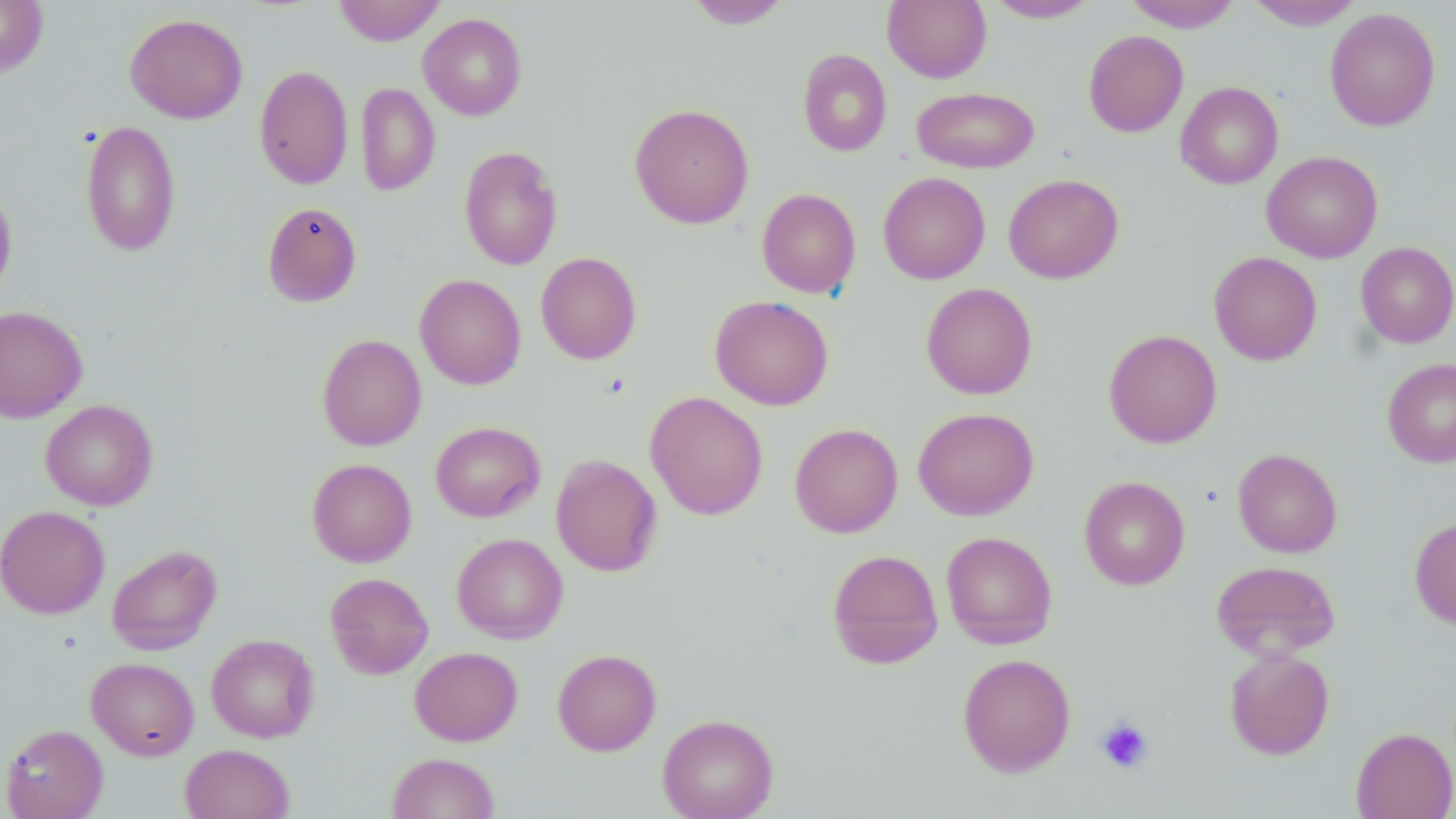

Approximate bounding boxes as named x1/y1/x2/y2 corners in pixels. Platelet locations: (x1=1096, y1=716, x2=1154, y2=774). Uninfected red blood cell locations: (x1=0, y1=0, x2=48, y2=76), (x1=333, y1=0, x2=445, y2=46), (x1=684, y1=0, x2=793, y2=29), (x1=882, y1=0, x2=991, y2=83), (x1=986, y1=0, x2=1100, y2=23), (x1=1124, y1=0, x2=1241, y2=32), (x1=1246, y1=0, x2=1364, y2=30), (x1=1324, y1=7, x2=1440, y2=132), (x1=125, y1=13, x2=248, y2=124), (x1=418, y1=13, x2=527, y2=121), (x1=1083, y1=30, x2=1188, y2=137), (x1=797, y1=49, x2=892, y2=157), (x1=254, y1=64, x2=353, y2=190), (x1=1175, y1=81, x2=1284, y2=189), (x1=356, y1=82, x2=440, y2=196), (x1=911, y1=86, x2=1039, y2=173), (x1=629, y1=102, x2=754, y2=230), (x1=80, y1=119, x2=182, y2=257), (x1=459, y1=146, x2=562, y2=270), (x1=1261, y1=151, x2=1383, y2=263), (x1=878, y1=171, x2=991, y2=284), (x1=1003, y1=173, x2=1124, y2=284), (x1=0, y1=183, x2=18, y2=299), (x1=757, y1=188, x2=861, y2=298), (x1=262, y1=201, x2=362, y2=307), (x1=1355, y1=242, x2=1456, y2=348), (x1=536, y1=251, x2=641, y2=364), (x1=1208, y1=251, x2=1322, y2=366), (x1=414, y1=273, x2=526, y2=390), (x1=921, y1=283, x2=1037, y2=399), (x1=710, y1=295, x2=833, y2=410), (x1=0, y1=305, x2=88, y2=422), (x1=1103, y1=329, x2=1222, y2=449), (x1=317, y1=334, x2=426, y2=451), (x1=1382, y1=359, x2=1456, y2=467), (x1=645, y1=391, x2=768, y2=520), (x1=40, y1=399, x2=158, y2=511), (x1=913, y1=407, x2=1039, y2=520), (x1=430, y1=421, x2=544, y2=522), (x1=789, y1=422, x2=903, y2=537), (x1=1232, y1=448, x2=1342, y2=558), (x1=551, y1=453, x2=662, y2=577), (x1=307, y1=458, x2=417, y2=567), (x1=1079, y1=476, x2=1190, y2=590), (x1=0, y1=505, x2=110, y2=618), (x1=1410, y1=517, x2=1456, y2=630), (x1=941, y1=531, x2=1058, y2=649), (x1=452, y1=532, x2=568, y2=643), (x1=106, y1=544, x2=222, y2=655), (x1=826, y1=549, x2=944, y2=669), (x1=1211, y1=560, x2=1340, y2=661), (x1=325, y1=572, x2=434, y2=679), (x1=206, y1=633, x2=319, y2=742), (x1=410, y1=646, x2=523, y2=746), (x1=552, y1=648, x2=661, y2=756), (x1=1224, y1=648, x2=1335, y2=760), (x1=957, y1=653, x2=1076, y2=776), (x1=86, y1=657, x2=199, y2=759), (x1=657, y1=713, x2=779, y2=819), (x1=0, y1=724, x2=108, y2=819), (x1=1350, y1=727, x2=1456, y2=819), (x1=180, y1=744, x2=295, y2=819), (x1=387, y1=752, x2=500, y2=818). Slide-level diagnosis: no evidence of blood parasites. Single field of view. Optical microscopy. 1000x magnification. May-Grünwald-Giemsa-stained preparation. Image is 1456×819 pixels. Thin blood smear.